Classify this cell by malaria status.
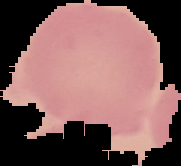

Uninfected.

{
  "preparation": "thin blood film",
  "image_type": "segmented cell region with the area outside set to black",
  "image_size": "181×166 pixels"
}